Classify this cell by malaria status.
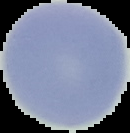
Uninfected.

Summary:
  - Preparation: thin blood film
  - Image size: 130×133 pixels
  - Image type: segmented cell region with the area outside set to black